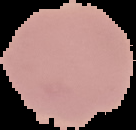
{
  "result": "no malaria parasites seen",
  "image_size": "136×130 pixels",
  "image_type": "segmented cell region on a black background",
  "preparation": "thin blood smear"
}